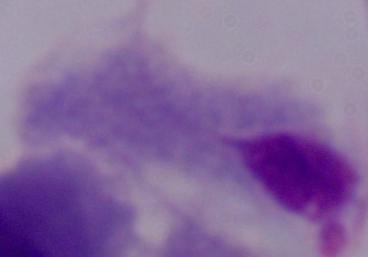

identification = trichomonad
magnification = 1000x
modality = micrograph